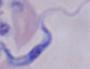

Summary:
  - Identification: trypanosome
  - Magnification: 1000x
  - Modality: micrograph